Outline every parasitised red blood cell.
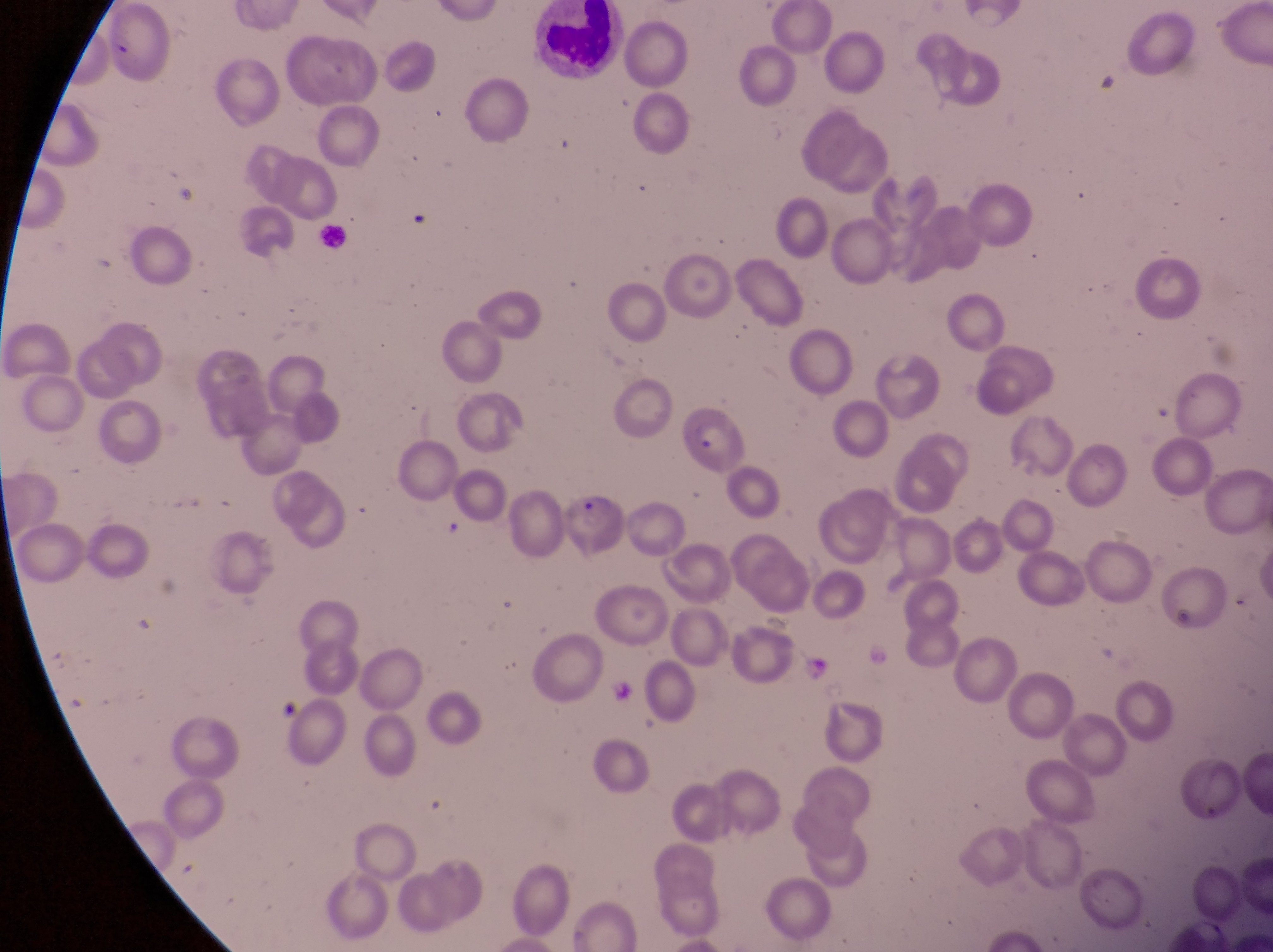
Approximate bounding boxes as [left, top, right, bottom] in pixels.
Parasitised red blood cells: [561, 482, 626, 559].

preparation = thin blood smear
leukocyte locations = approximate bounding boxes as [left, top, right, bottom] in pixels: [532, 3, 636, 86], [317, 225, 346, 252]
capture = smartphone photograph through the eyepiece of an Olympus CX-23 microscope
image size = 1273×952 pixels
field of view = single
country = Uganda
magnification = 1000x